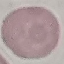

Result: no malaria parasites detected. Automatically extracted cell patch, resized to 64 × 64 pixels. Giemsa-stained preparation. Thin blood film. Photographed with a smartphone camera at the microscope eyepiece.